Give the extent of all Plasmodium falciparum-infected red blood cells.
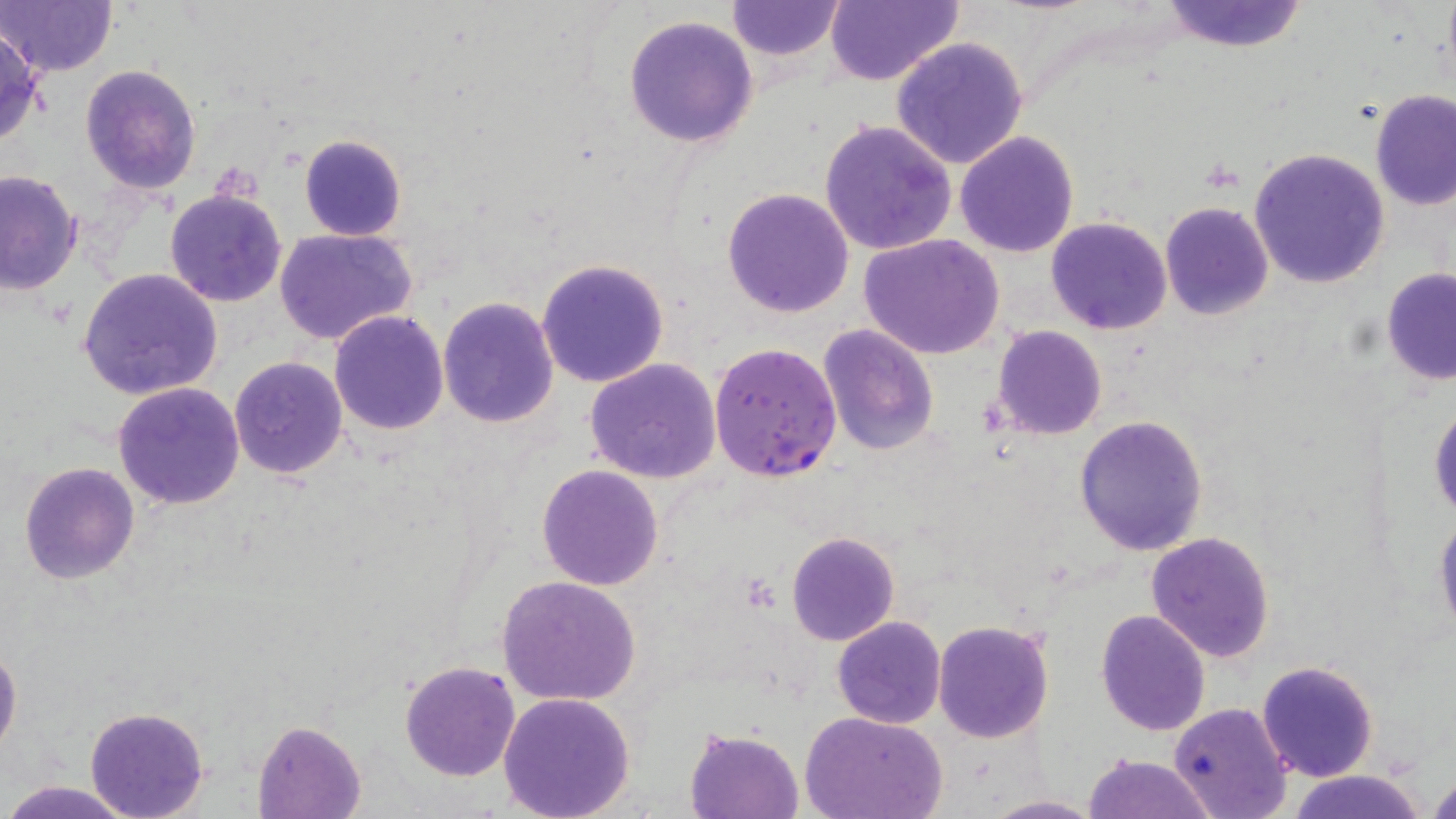
Approximate bounding boxes as [x1, y1, x2, y2] in pixels.
Plasmodium falciparum-infected red blood cells: [710, 342, 843, 484].

Summary:
  - Uninfected red blood cell locations: [0, 0, 121, 78], [726, 0, 846, 60], [823, 1, 962, 87], [1158, 1, 1308, 52], [623, 14, 760, 148], [0, 25, 45, 146], [890, 36, 1029, 171], [80, 64, 201, 195], [1368, 92, 1456, 211], [818, 119, 957, 255], [955, 131, 1079, 258], [297, 133, 405, 241], [1249, 147, 1390, 289], [0, 169, 81, 295], [722, 186, 854, 318], [165, 189, 288, 309], [1160, 203, 1273, 319], [1046, 216, 1172, 335], [275, 228, 417, 348], [860, 233, 1005, 358], [537, 257, 670, 389], [78, 267, 223, 400], [1381, 269, 1456, 384], [437, 297, 559, 429], [330, 310, 450, 435], [820, 325, 940, 456], [992, 326, 1108, 440], [228, 356, 347, 478], [585, 359, 721, 483], [112, 381, 245, 511], [1429, 397, 1456, 521], [1074, 416, 1208, 556], [19, 463, 140, 585], [537, 463, 665, 590], [1433, 514, 1456, 637], [787, 531, 899, 646], [1145, 531, 1276, 662], [497, 575, 641, 705], [1096, 609, 1211, 735], [831, 616, 945, 728], [933, 620, 1054, 742], [0, 644, 22, 757], [398, 660, 521, 782], [1256, 660, 1379, 782], [497, 692, 637, 819], [1168, 702, 1294, 819], [85, 707, 209, 819], [801, 711, 948, 819], [253, 719, 368, 819], [686, 727, 804, 818], [1081, 752, 1218, 819], [1282, 772, 1429, 819], [1426, 773, 1456, 818], [4, 779, 132, 819], [981, 795, 1104, 818]
  - Slide-level diagnosis: Plasmodium falciparum
  - Modality: optical microscopy
  - Magnification: 1000x
  - Field of view: single
  - Image size: 1456×819 pixels
  - Stain: May-Grünwald-Giemsa
  - Preparation: thin blood film